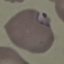
Result: malaria parasites detected. Cell patch, automatically extracted from a larger field of view and resized to 64 × 64 pixels. Giemsa-stained preparation. Acquired by smartphone through the microscope eyepiece. Thin blood smear.